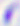

Photomicrograph. Toxoplasma gondii is seen. Captured at 400x magnification.